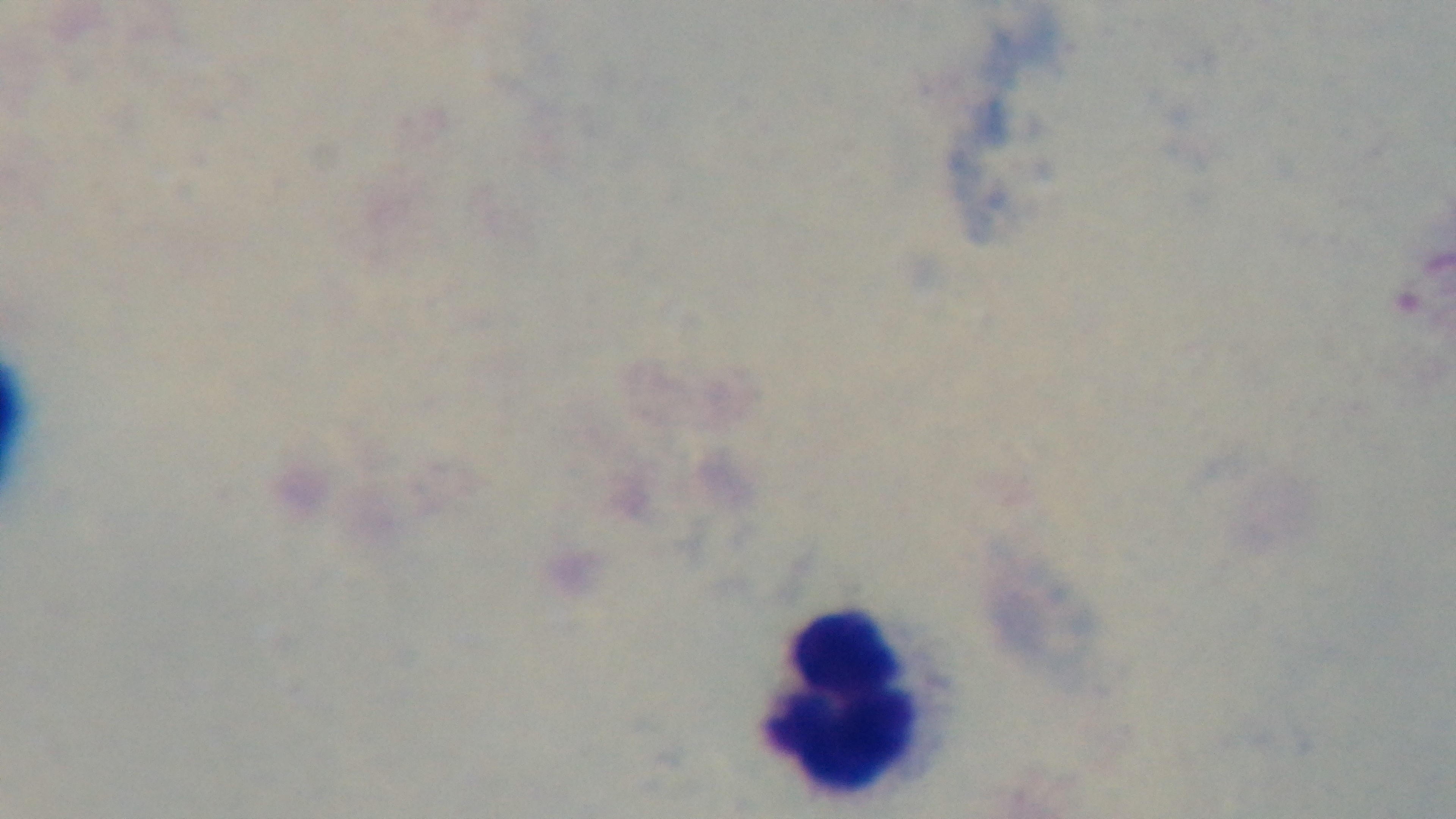
Summary:
  - Malaria status: uninfected
  - Objective: 100x oil immersion
  - Capture: mounted 4K digital camera
  - Field of view: single
  - Modality: light microscopy
  - Preparation: thick smear
  - Stain: Giemsa